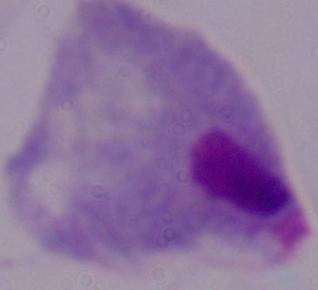
Summary:
  - Identification: trichomonad
  - Magnification: 1000x
  - Modality: micrograph